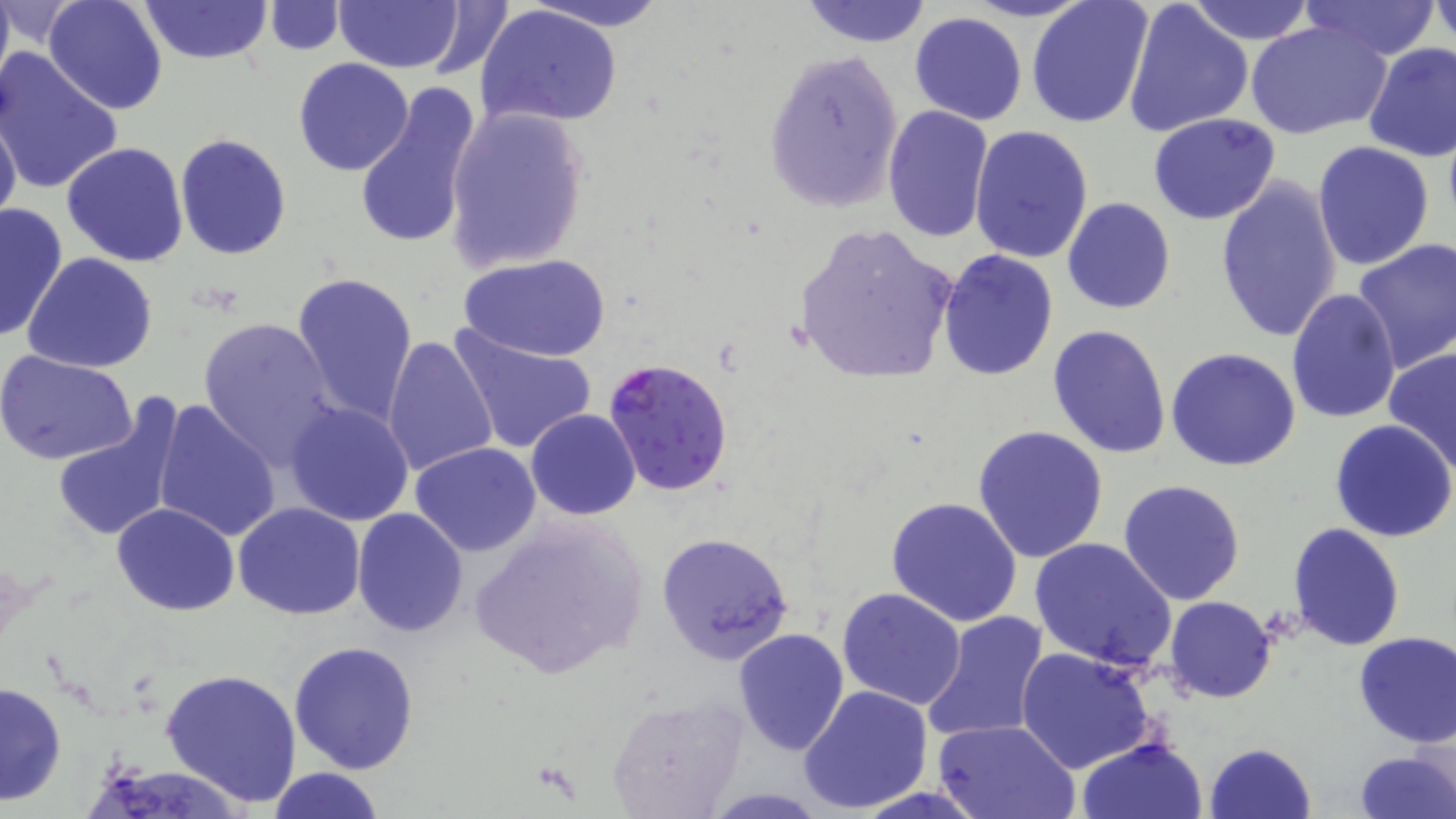
slide-level diagnosis = Plasmodium falciparum
magnification = 1000x
uninfected red blood cell locations = approximate bounding boxes as (x1,y1)-(x2,y2) corner pairs in pixels: (0,0)-(15,99), (44,0)-(167,116), (137,0)-(273,65), (521,0)-(672,32), (800,0)-(934,48), (1123,0)-(1255,138), (262,1)-(343,54), (332,1)-(464,73), (419,1)-(517,83), (1026,1)-(1154,129), (1184,1)-(1318,45), (1300,1)-(1438,61), (1432,1)-(1456,49), (474,4)-(624,128), (909,12)-(1029,126), (1245,19)-(1392,141), (1362,42)-(1456,164), (761,47)-(905,213), (1,48)-(124,197), (293,58)-(414,176), (354,82)-(483,251), (442,103)-(592,274), (882,106)-(995,245), (0,107)-(23,227), (1147,113)-(1281,224), (970,126)-(1094,265), (174,133)-(292,260), (61,141)-(189,268), (1312,141)-(1435,269), (1214,175)-(1343,345), (1062,197)-(1175,314), (0,200)-(70,344), (792,222)-(958,384), (1352,236)-(1456,377), (938,250)-(1059,380), (23,253)-(159,373), (460,253)-(609,362), (291,272)-(418,423), (1287,289)-(1402,425), (197,315)-(342,468), (1048,325)-(1172,459), (446,326)-(598,456), (384,335)-(500,479), (1383,346)-(1456,478), (1166,347)-(1301,471), (0,350)-(137,464), (50,397)-(186,546), (152,399)-(281,543), (286,402)-(413,526), (525,409)-(642,520), (1330,418)-(1456,542), (974,424)-(1109,563), (410,442)-(542,556), (1118,480)-(1246,606), (886,496)-(1023,627), (233,502)-(366,621), (112,503)-(240,617), (352,508)-(469,636), (465,518)-(648,682), (1288,522)-(1405,651), (656,531)-(797,666), (1030,536)-(1176,671), (837,588)-(967,712), (1165,596)-(1275,704), (920,610)-(1051,744), (733,628)-(849,755), (1353,631)-(1456,747), (289,640)-(418,774), (1016,646)-(1156,774), (161,668)-(302,807), (1,679)-(66,807), (800,684)-(933,814), (606,694)-(748,818), (933,719)-(1081,819), (1077,737)-(1208,819), (1204,742)-(1316,819), (1351,749)-(1455,819), (268,767)-(384,819)
Plasmodium falciparum-infected red blood cell locations = approximate bounding boxes as (x1,y1)-(x2,y2) corner pairs in pixels: (603,357)-(734,495)
preparation = thin blood film
stain = May-Grünwald-Giemsa
modality = optical microscopy
field of view = one of a larger specimen
image size = 1456×819 pixels